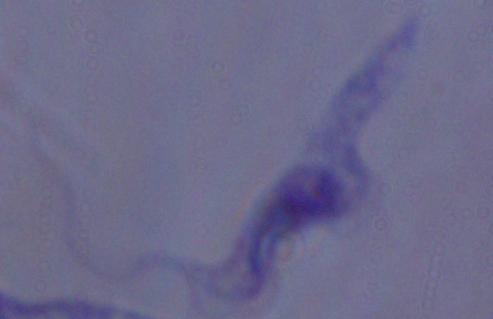
Photomicrograph. Captured at 1000x magnification. A trypanosome is shown.